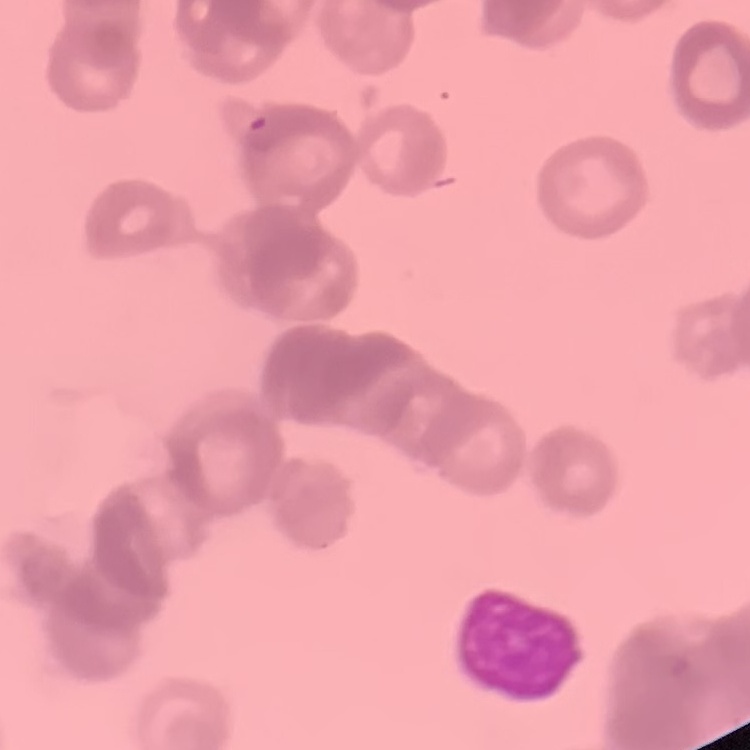
Summary:
  - Red blood cell morphology: rouleaux formation
  - Image type: square crop of a larger photomicrograph
  - Preparation: thin blood film
  - Stain: Field's or Giemsa